Report the malaria status of this cell.
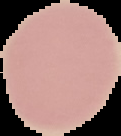

It is uninfected.

preparation = thin blood smear
image size = 121×136 pixels
image type = cell region segmented out of the field of view; surrounding area masked to black